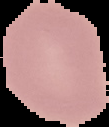

Summary:
  - Image size: 109×127 pixels
  - Preparation: thin blood film
  - Result: no Plasmodium parasites seen
  - Image type: segmented cell region on a black background